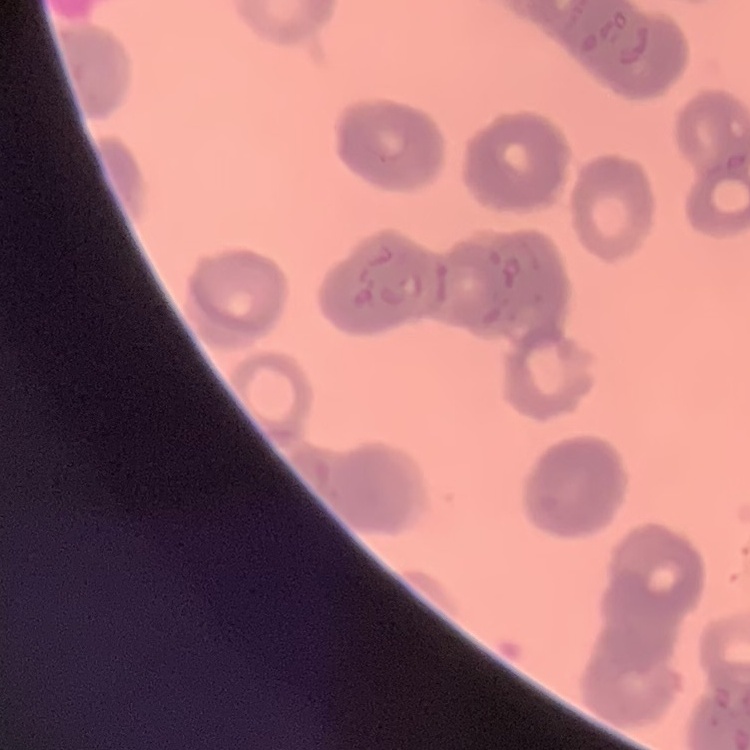
Summary:
  - Erythrocyte morphology: rouleaux formation
  - Stain: Field's or Giemsa
  - Image type: one tile cut from a larger photomicrograph
  - Preparation: thin peripheral smear